Name the parasite shown.
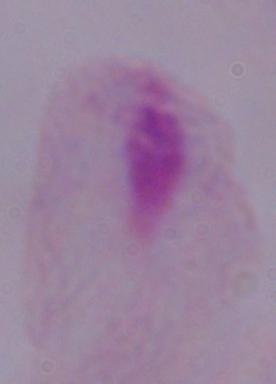
This is a trichomonad.

Micrograph. 1000x magnification.